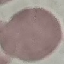

Malaria status: uninfected. Giemsa stain. Thin blood film. Automatically extracted cell patch, resized to 64 × 64 pixels. Photographed with a smartphone camera at the microscope eyepiece.